Identify the blood parasite species.
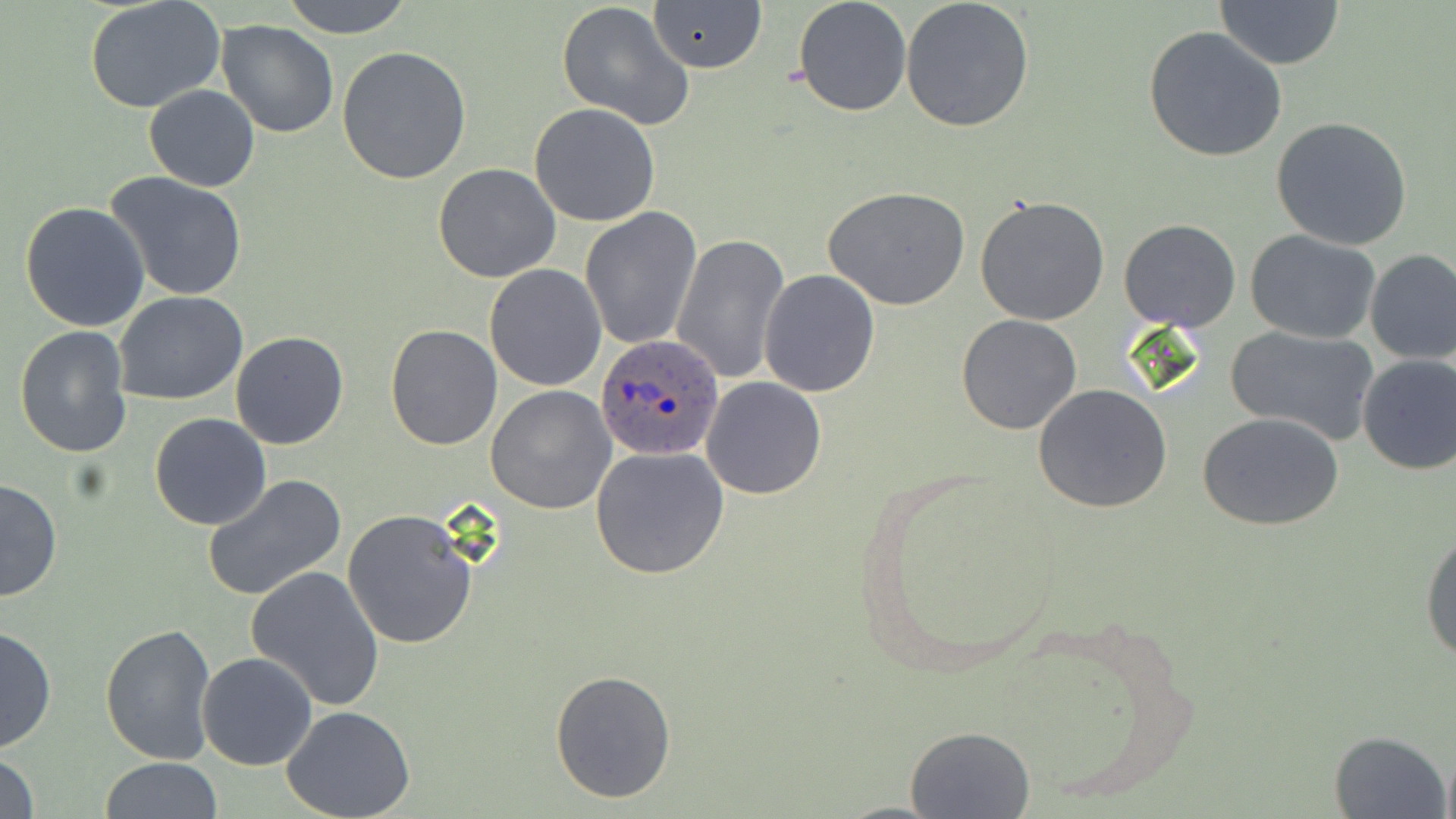

Plasmodium ovale.

magnification = 1000x
modality = optical microscopy
uninfected red blood cell locations = approximate bounding boxes as named x1/y1/x2/y2 corners in pixels: (x1=280, y1=0, x2=415, y2=39), (x1=793, y1=0, x2=912, y2=118), (x1=900, y1=0, x2=1035, y2=133), (x1=84, y1=1, x2=225, y2=113), (x1=1215, y1=1, x2=1345, y2=70), (x1=558, y1=2, x2=692, y2=129), (x1=648, y1=2, x2=767, y2=74), (x1=216, y1=19, x2=339, y2=138), (x1=1143, y1=26, x2=1287, y2=162), (x1=336, y1=45, x2=472, y2=184), (x1=144, y1=84, x2=260, y2=192), (x1=529, y1=103, x2=660, y2=226), (x1=1271, y1=117, x2=1413, y2=252), (x1=432, y1=163, x2=561, y2=283), (x1=104, y1=171, x2=249, y2=302), (x1=825, y1=187, x2=971, y2=311), (x1=974, y1=195, x2=1110, y2=324), (x1=20, y1=202, x2=151, y2=333), (x1=580, y1=208, x2=701, y2=350), (x1=1118, y1=218, x2=1240, y2=332), (x1=1245, y1=229, x2=1382, y2=345), (x1=671, y1=232, x2=789, y2=387), (x1=1364, y1=249, x2=1456, y2=365), (x1=483, y1=263, x2=607, y2=392), (x1=759, y1=270, x2=880, y2=397), (x1=114, y1=293, x2=248, y2=406), (x1=956, y1=314, x2=1083, y2=434), (x1=15, y1=325, x2=133, y2=458), (x1=385, y1=325, x2=501, y2=448), (x1=1226, y1=325, x2=1380, y2=446), (x1=230, y1=331, x2=349, y2=450), (x1=1356, y1=354, x2=1456, y2=475), (x1=700, y1=376, x2=827, y2=500), (x1=1032, y1=384, x2=1174, y2=515), (x1=486, y1=385, x2=617, y2=515), (x1=149, y1=412, x2=271, y2=531), (x1=1199, y1=412, x2=1345, y2=531), (x1=589, y1=445, x2=732, y2=581), (x1=202, y1=474, x2=347, y2=601), (x1=0, y1=479, x2=61, y2=603), (x1=342, y1=509, x2=478, y2=650), (x1=1421, y1=531, x2=1456, y2=665), (x1=246, y1=565, x2=386, y2=710), (x1=99, y1=623, x2=217, y2=765), (x1=0, y1=625, x2=56, y2=755), (x1=196, y1=652, x2=318, y2=771), (x1=549, y1=668, x2=678, y2=804), (x1=282, y1=706, x2=416, y2=818), (x1=905, y1=725, x2=1034, y2=818), (x1=1329, y1=731, x2=1452, y2=819), (x1=1440, y1=749, x2=1456, y2=819), (x1=0, y1=750, x2=40, y2=819), (x1=99, y1=756, x2=222, y2=819)
image size = 1456×819 pixels
stain = May-Grünwald-Giemsa
field of view = single
preparation = thin blood film
Plasmodium ovale-infected red blood cell locations = approximate bounding boxes as named x1/y1/x2/y2 corners in pixels: (x1=595, y1=332, x2=728, y2=461)